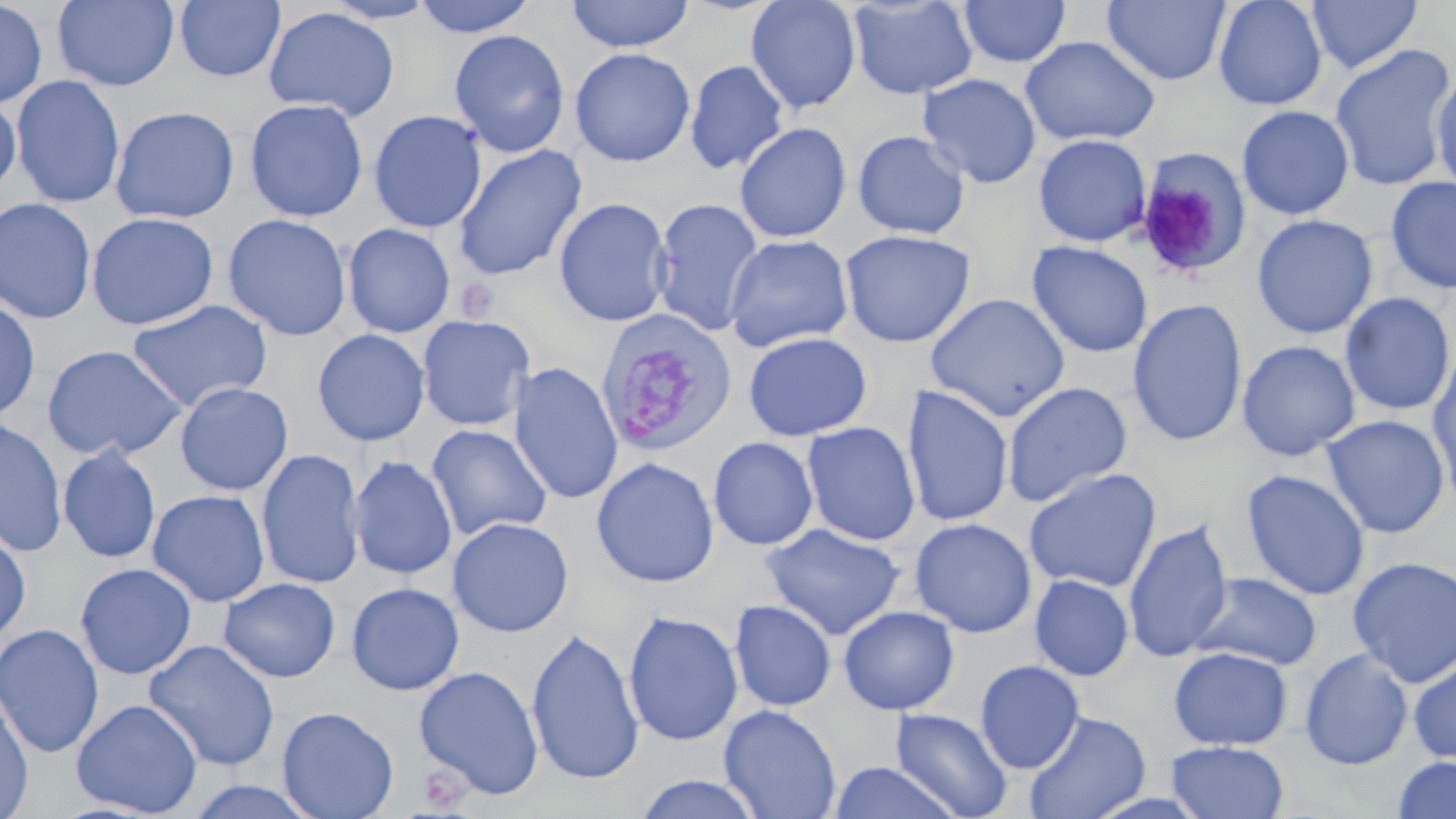
Approximate bounding boxes as (x1, y1, x2, y2) in pixels. Uninfected red blood cell locations: (0, 0, 48, 110), (53, 0, 180, 90), (173, 0, 286, 82), (319, 0, 442, 24), (411, 0, 539, 37), (564, 0, 696, 53), (745, 0, 862, 114), (847, 0, 978, 99), (958, 0, 1071, 68), (1101, 0, 1231, 86), (1213, 0, 1327, 110), (1306, 0, 1423, 74), (263, 6, 400, 121), (448, 29, 570, 158), (1019, 36, 1160, 146), (1330, 44, 1455, 191), (569, 47, 696, 167), (685, 59, 789, 174), (1430, 70, 1456, 196), (918, 74, 1042, 188), (11, 75, 126, 209), (0, 96, 21, 198), (245, 98, 368, 222), (110, 105, 240, 224), (1237, 105, 1355, 220), (369, 110, 487, 233), (734, 122, 852, 243), (852, 129, 971, 240), (1033, 133, 1151, 247), (453, 144, 587, 281), (1132, 154, 1251, 276), (1385, 176, 1456, 295), (0, 197, 97, 324), (554, 197, 673, 327), (650, 198, 765, 337), (86, 212, 219, 331), (222, 213, 352, 341), (1252, 214, 1378, 340), (342, 223, 456, 338), (839, 228, 975, 348), (723, 234, 855, 353), (1027, 241, 1153, 358), (1339, 292, 1455, 416), (924, 293, 1071, 422), (0, 296, 41, 422), (125, 299, 273, 413), (1127, 299, 1248, 448), (417, 314, 536, 432), (312, 328, 430, 446), (743, 331, 872, 441), (1237, 340, 1360, 461), (41, 343, 188, 461), (1427, 345, 1456, 500), (508, 361, 624, 505), (1001, 381, 1133, 508), (174, 382, 293, 496), (900, 384, 1014, 528), (1322, 414, 1450, 539), (0, 416, 67, 557), (801, 421, 921, 546), (426, 424, 552, 541), (708, 436, 819, 551), (58, 444, 162, 564), (256, 449, 366, 589), (348, 454, 458, 580), (591, 457, 719, 588), (1023, 468, 1162, 592), (1241, 469, 1370, 601), (147, 489, 270, 608), (447, 516, 574, 637), (910, 517, 1036, 638), (1123, 519, 1233, 663), (761, 523, 905, 640), (0, 526, 32, 645), (1347, 556, 1456, 687), (75, 563, 197, 680), (1191, 573, 1322, 670), (1030, 574, 1134, 681), (218, 577, 341, 683), (346, 582, 464, 695), (729, 600, 837, 712), (838, 605, 959, 715), (623, 610, 744, 746), (0, 623, 105, 758), (526, 628, 644, 787), (144, 638, 281, 771), (1169, 646, 1293, 750), (1299, 649, 1413, 770), (1408, 652, 1456, 766), (975, 660, 1085, 774), (414, 665, 544, 800), (0, 688, 34, 819), (71, 698, 203, 816), (719, 704, 841, 818), (277, 705, 399, 818), (890, 707, 1013, 819), (1023, 710, 1151, 819), (1165, 741, 1289, 819), (1391, 755, 1456, 819), (826, 761, 964, 819), (631, 774, 763, 818), (181, 779, 325, 819). Plasmodium vivax-infected red blood cell locations: (595, 309, 738, 457). Platelet locations: (455, 278, 498, 323), (417, 763, 472, 812). Slide-level diagnosis: Plasmodium vivax. 1000x magnification. Light microscopy. Single field of view. May-Grünwald-Giemsa-stained preparation. Image is 1456×819 pixels. Thin blood film.